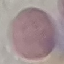

malaria status = uninfected
stain = Giemsa
capture = smartphone through the microscope eyepiece
preparation = thin smear
image type = cell patch, automatically extracted from a larger field of view and resized to 64 × 64 pixels